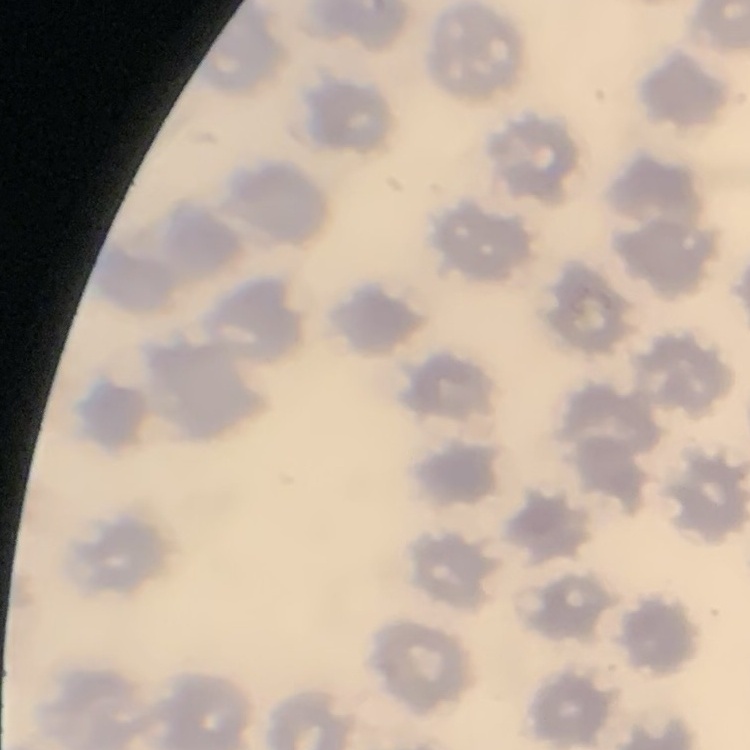 The red blood cells show no rouleaux formation. Stained with either Field's or Giemsa. Thin blood smear. One tile cut from a larger photomicrograph.